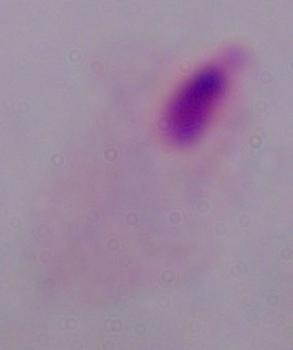
A trichomonad is shown. Photomicrograph. 1000x magnification.